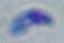

Summary:
  - Modality: photomicrograph
  - Identification: Toxoplasma gondii
  - Magnification: 1000x